Report the malaria status of this cell.
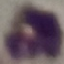
Uninfected.

Giemsa stain. Automatically extracted cell patch, resized to 64 × 64 pixels. Thin blood smear. Photographed with a smartphone camera at the microscope eyepiece.